Describe the morphology of the red blood cells.
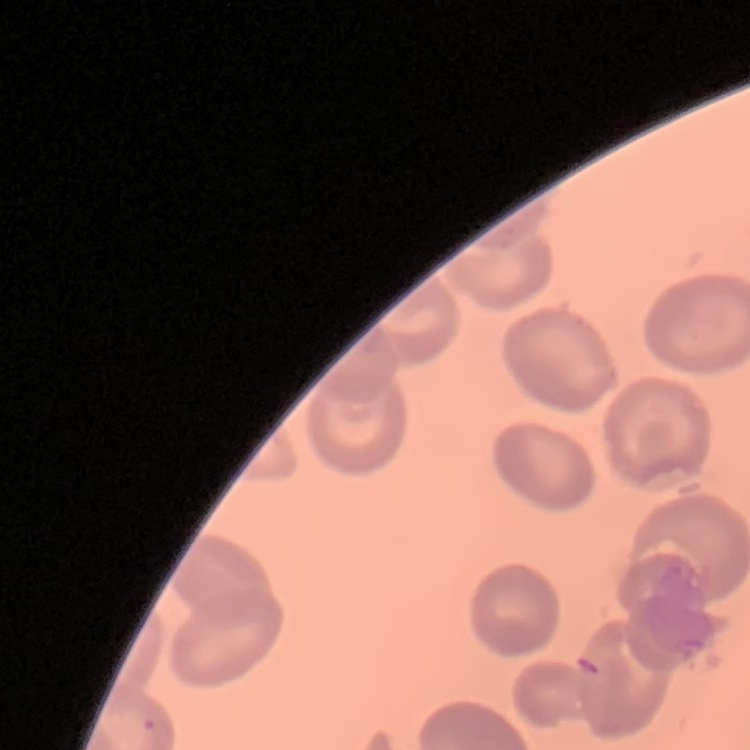

They show no rouleaux formation.

Summary:
  - Preparation: thin peripheral smear
  - Stain: Field's or Giemsa
  - Image type: square crop of a larger photomicrograph